Describe the morphology of the erythrocytes.
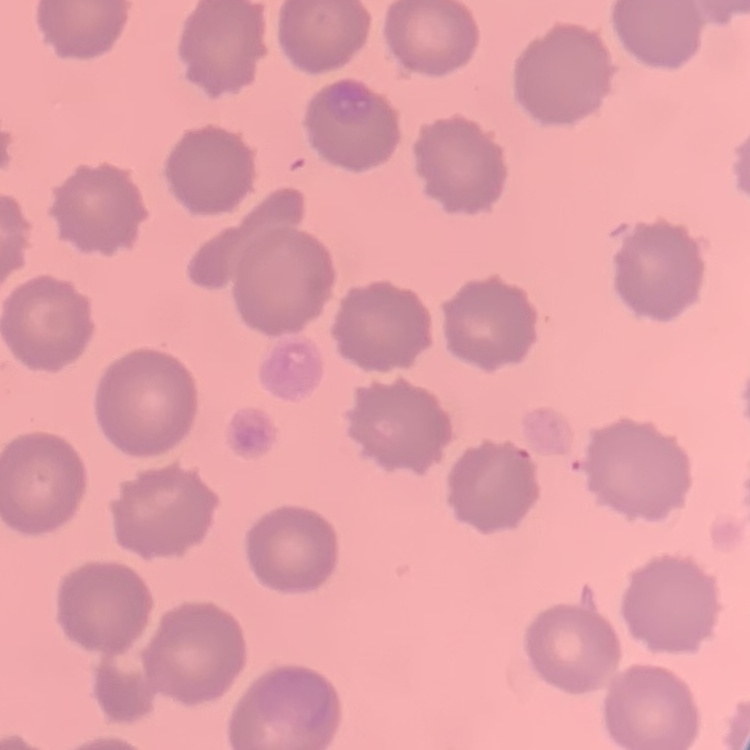

They show no rouleaux formation.

Summary:
  - Image type: one tile cut from a larger photomicrograph
  - Preparation: thin peripheral smear
  - Stain: Field's or Giemsa